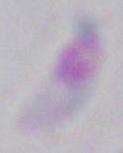
magnification: 1000x
modality: micrograph
identification: Toxoplasma gondii